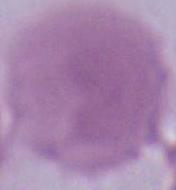
identification = erythrocyte
magnification = 1000x
modality = micrograph